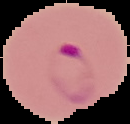
Cell region segmented out of the field of view; the surrounding area is masked to black. From a thin blood smear. Image is 130×124 pixels. Malaria status: parasitized.